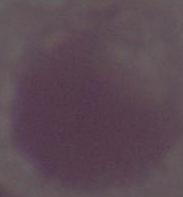 Captured at 1000x magnification. A red blood cell is seen. Micrograph.